Assess the morphology of the red blood cells.
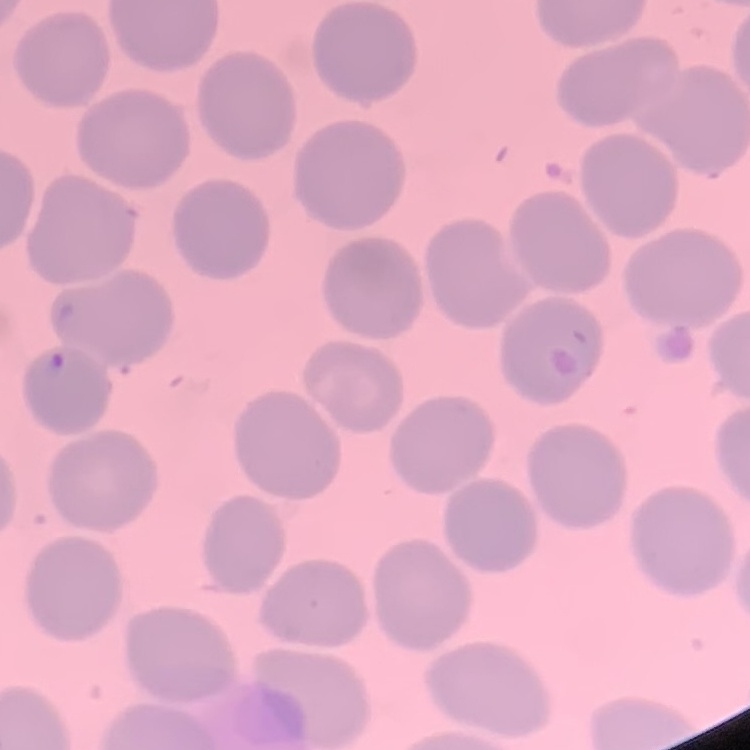
No rouleaux formation.

Field's or Giemsa stain. Thin blood film. One tile cut from a larger photomicrograph.